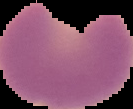
image size = 133×109 pixels
malaria status = parasitized
image type = segmented cell region with the area outside set to black
preparation = thin blood film